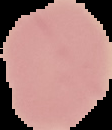

image type = segmented cell region on a black background
image size = 112×130 pixels
preparation = thin blood smear
malaria status = uninfected